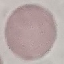

result: no malaria parasites detected
capture: smartphone through the microscope eyepiece
image_type: automatically extracted cell patch, resized to 64 × 64 pixels
preparation: thin blood smear
stain: Giemsa